Name the cell type shown.
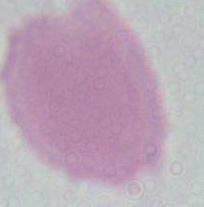
This is an erythrocyte.

Micrograph. 1000x magnification.